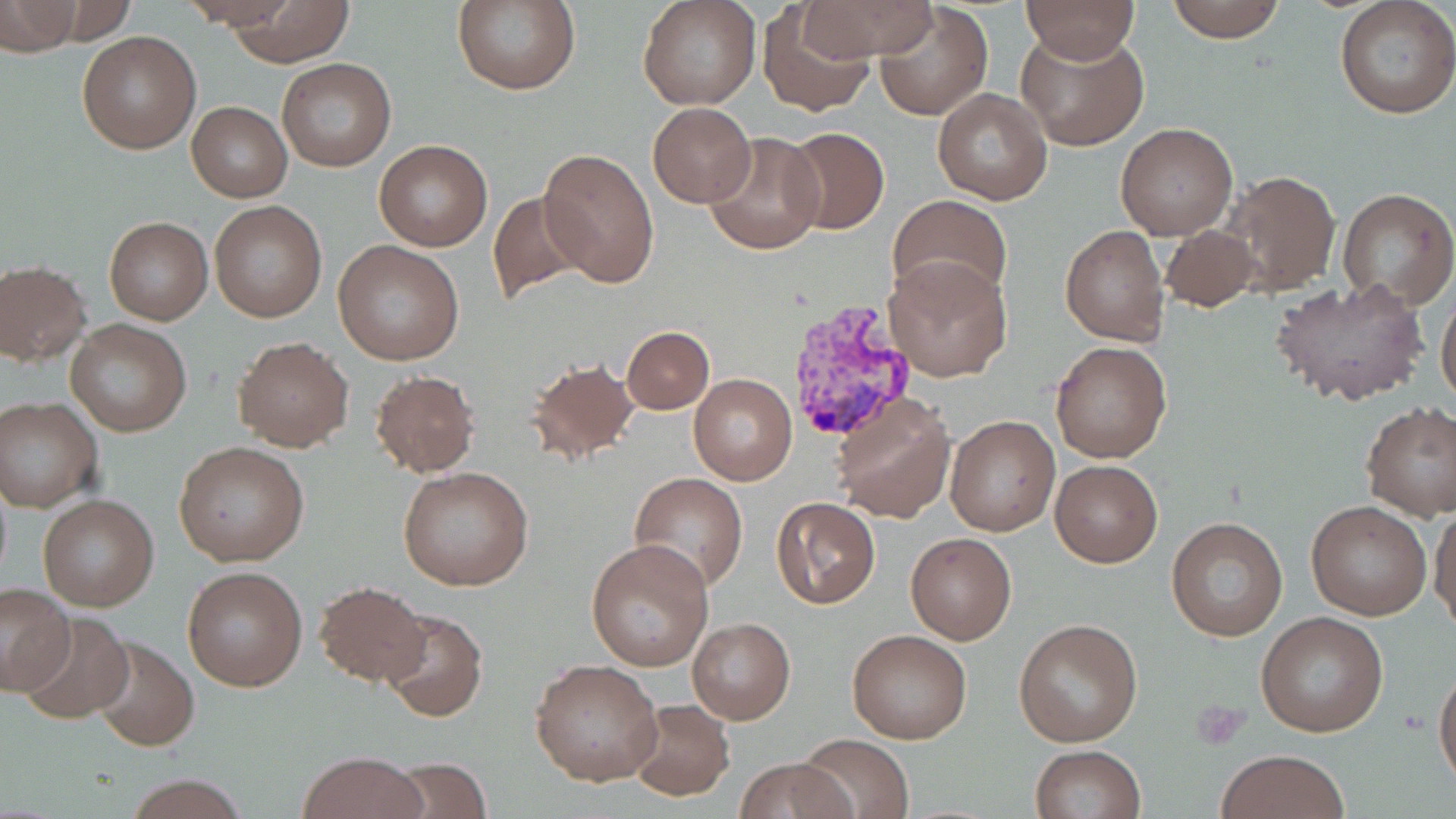
Summary:
  - Coordinate format: approximate bounding boxes as (x1,y1)-(x2,y2) corner pairs in pixels
  - Uninfected red blood cell locations: (223,0)-(355,65), (450,0)-(581,95), (638,0)-(761,110), (794,0)-(938,61), (1019,0)-(1141,65), (1164,0)-(1287,43), (3,2)-(80,53), (1334,2)-(1456,119), (873,4)-(993,122), (760,7)-(875,118), (76,30)-(203,154), (1017,31)-(1149,151), (276,58)-(397,171), (931,88)-(1053,205), (187,102)-(292,201), (647,103)-(757,208), (1114,123)-(1237,240), (781,126)-(889,235), (703,132)-(825,256), (374,138)-(493,251), (539,146)-(658,289), (1223,169)-(1341,295), (1336,188)-(1456,310), (486,190)-(595,306), (887,194)-(1013,306), (209,202)-(327,322), (103,216)-(212,324), (1161,224)-(1262,312), (1060,225)-(1169,347), (332,240)-(464,366), (884,257)-(1012,381), (0,260)-(91,365), (1271,275)-(1429,408), (1436,292)-(1456,411), (66,320)-(191,437), (622,326)-(714,413), (233,336)-(353,451), (1050,341)-(1173,464), (523,356)-(643,468), (370,368)-(480,478), (687,374)-(797,485), (830,390)-(957,522), (0,396)-(104,512), (1361,401)-(1456,521), (945,415)-(1059,537), (173,441)-(309,565), (1050,459)-(1162,567), (398,465)-(535,592), (628,473)-(748,593), (38,494)-(159,611), (770,497)-(881,609), (1305,499)-(1432,620), (1430,501)-(1456,632), (1167,517)-(1289,639), (905,533)-(1016,644), (585,537)-(714,670), (182,565)-(308,692), (314,578)-(430,687), (0,584)-(76,694), (379,608)-(488,722), (16,613)-(136,726), (1256,613)-(1387,737), (688,616)-(795,724), (1013,618)-(1143,747), (847,628)-(973,744), (88,636)-(199,752), (530,659)-(662,787), (1433,666)-(1456,793), (626,700)-(734,801), (795,733)-(913,819), (1029,745)-(1145,819), (1215,748)-(1350,819), (298,751)-(425,819), (383,756)-(495,818), (732,757)-(856,818), (122,772)-(250,819)
  - Plasmodium vivax-infected red blood cell locations: (784,299)-(921,442)
  - Platelet locations: (1192,698)-(1249,747)
  - Slide-level diagnosis: Plasmodium vivax
  - Preparation: thin blood smear
  - Modality: optical microscopy
  - Magnification: 1000x
  - Field of view: single
  - Image size: 1456×819 pixels
  - Stain: May-Grünwald-Giemsa